Classify the preparation.
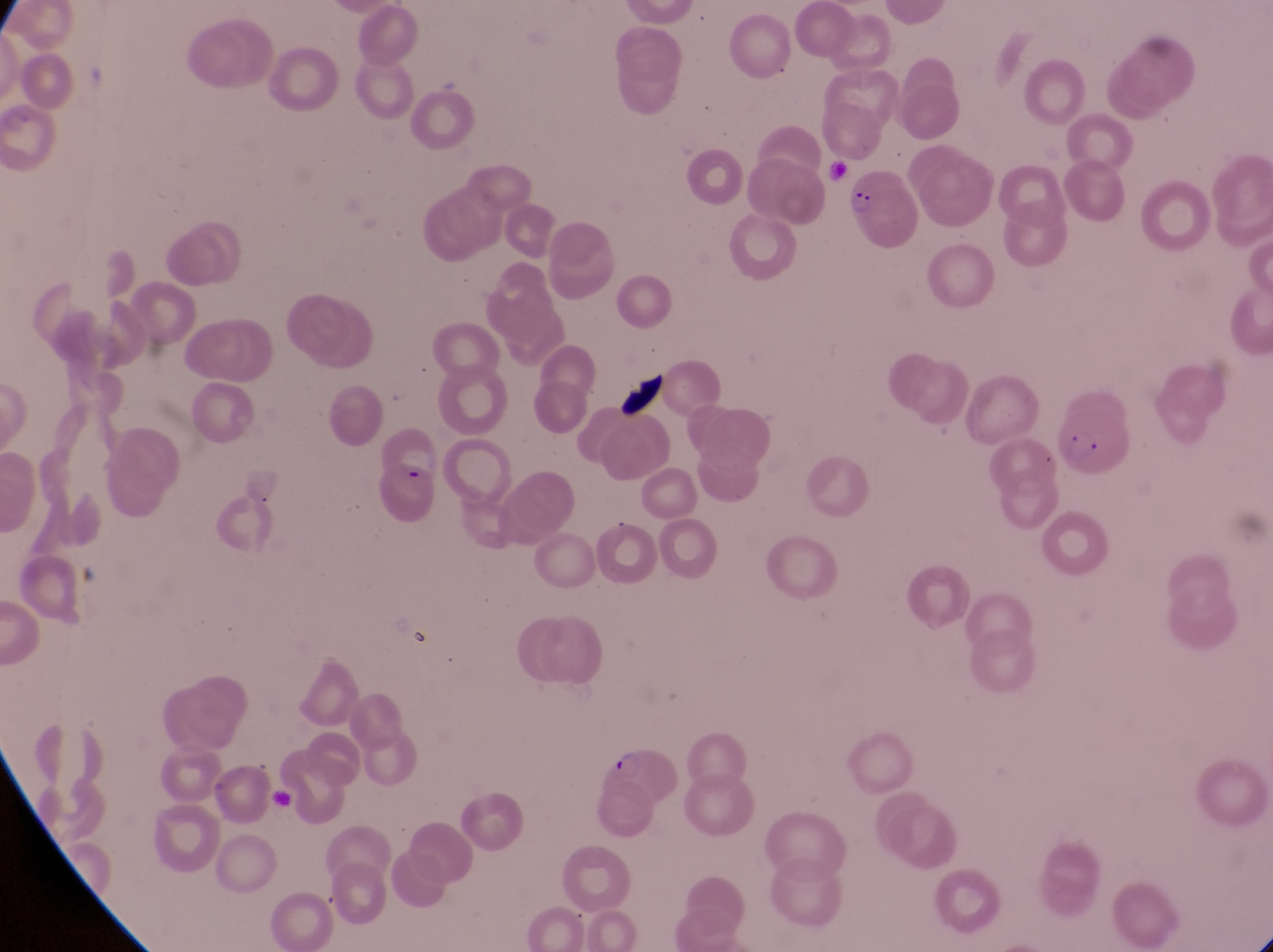

Thin blood smear.

Approximate bounding boxes as [left, top, right, bottom] in pixels.
Summary:
  - Parasitised red blood cell locations: [843, 162, 925, 250], [1060, 399, 1123, 474], [601, 742, 677, 805]
  - Artifact (platelet-like body, stain precipitate, or debris) locations: [611, 375, 671, 422]
  - Image size: 1273×952 pixels
  - Magnification: 1000x
  - Capture: smartphone photograph through the eyepiece of an Olympus CX-23 microscope
  - Field of view: single
  - Country: Uganda